Report the malaria status of this cell.
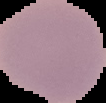

Uninfected.

image type = segmented cell region with the area outside set to black
image size = 106×103 pixels
preparation = thin blood film